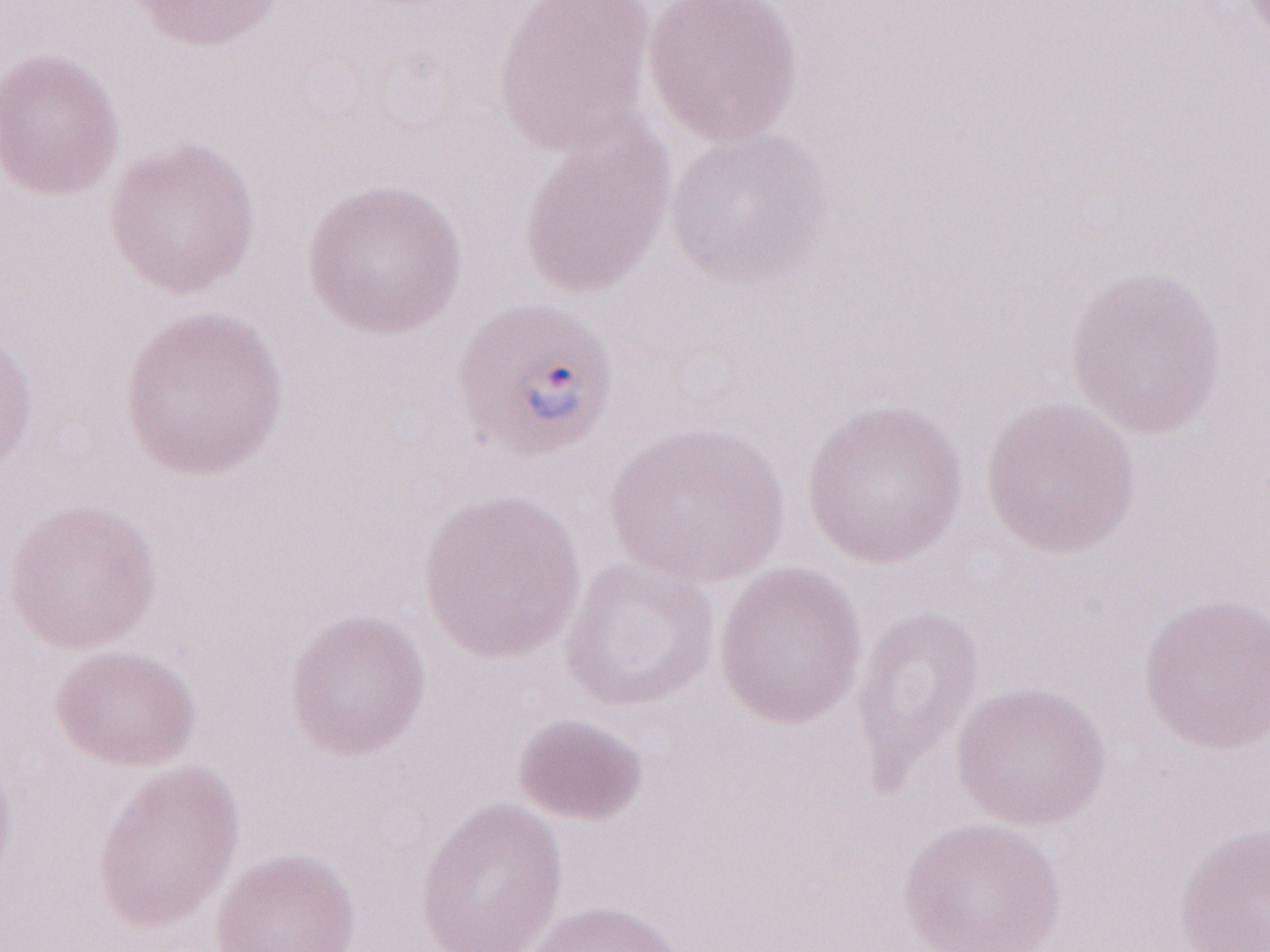 Thin blood film. May-Grünwald-Giemsa (MGG) stain. One field of this slide. Image is 1270×952 pixels. Olympus BX43 microscope, Olympus DP73 camera. Patient-level malaria diagnosis: positive. 1,000x magnification.